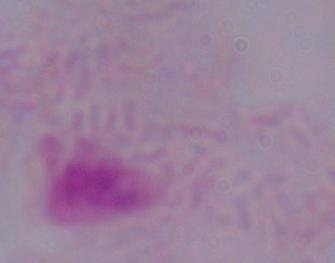
Summary:
  - Identification: trichomonad
  - Magnification: 1000x
  - Modality: micrograph